Locate every blood parasite and identify its species.
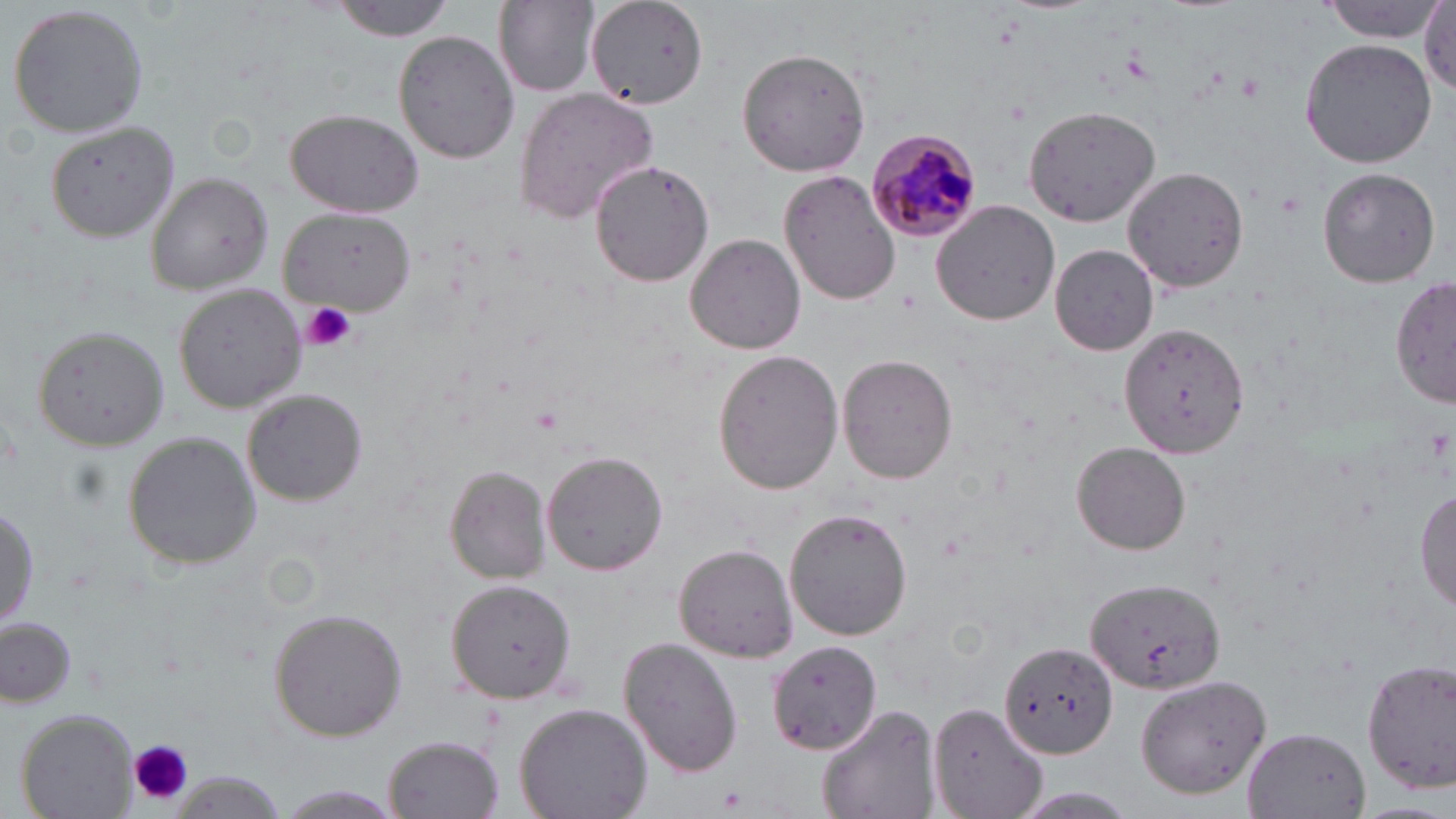
Approximate bounding boxes as (x1,y1)-(x2,y2) corner pairs in pixels.
Plasmodium malariae-infected red blood cells: (868,131)-(986,240).
No Plasmodium falciparum, Plasmodium ovale, Plasmodium vivax, Babesia divergens, or Trypanosoma brucei observed.

Summary:
  - Platelet locations: (1238,73)-(1265,100), (303,300)-(356,353), (530,404)-(565,433), (128,737)-(191,805), (716,785)-(749,813)
  - Uninfected red blood cell locations: (493,0)-(599,98), (587,0)-(710,110), (1321,0)-(1444,40), (328,1)-(457,40), (6,3)-(151,140), (1421,4)-(1456,98), (393,30)-(519,165), (1300,38)-(1436,168), (737,47)-(874,177), (514,87)-(661,221), (1023,105)-(1164,224), (284,107)-(424,217), (44,122)-(181,243), (588,160)-(716,286), (1124,168)-(1249,291), (1316,168)-(1440,287), (780,171)-(901,306), (146,172)-(273,295), (930,200)-(1060,326), (279,209)-(416,314), (684,232)-(806,354), (1050,244)-(1159,354), (1392,275)-(1456,409), (173,283)-(306,414), (1121,322)-(1247,457), (31,325)-(169,451), (711,349)-(843,493), (836,354)-(959,484), (242,389)-(368,505), (122,430)-(260,572), (1071,441)-(1191,555), (541,450)-(668,576), (444,466)-(551,586), (1415,486)-(1455,611), (0,500)-(38,634), (783,507)-(914,641), (674,543)-(799,661), (444,575)-(577,704), (1086,577)-(1226,696), (267,607)-(407,742), (0,616)-(79,709), (619,637)-(742,777), (767,639)-(882,756), (1003,641)-(1118,759), (1361,655)-(1456,795), (1135,675)-(1275,800), (928,700)-(1047,819), (514,702)-(653,819), (816,704)-(939,819), (15,709)-(139,818), (1243,727)-(1370,819), (384,735)-(504,818), (168,773)-(290,819), (273,785)-(406,816), (1004,788)-(1144,819)
  - Slide-level diagnosis: Plasmodium malariae
  - Field of view: one of a larger specimen
  - Stain: May-Grünwald-Giemsa
  - Magnification: 1000x
  - Image size: 1456×819 pixels
  - Preparation: thin blood film
  - Modality: light microscopy